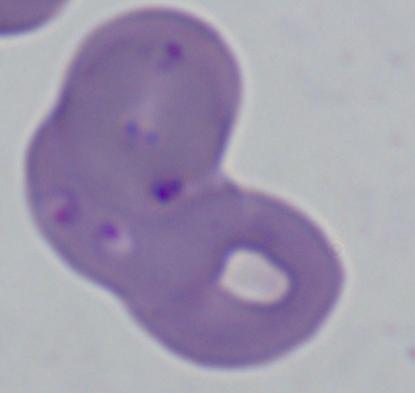

identification: Babesia
magnification: 1000x
modality: photomicrograph